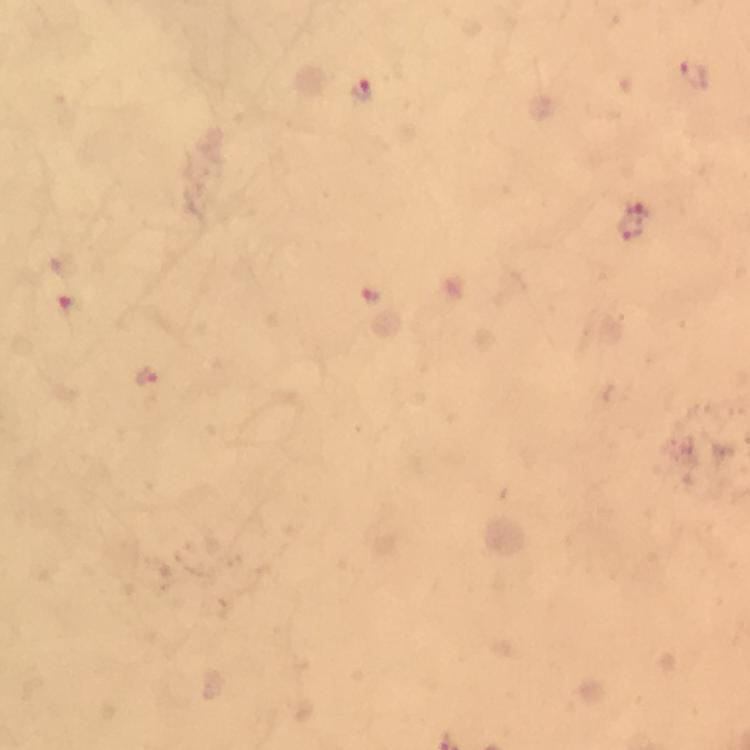
Approximate centers as (x, y) in pixels. Plasmodium parasite locations: (697, 76), (362, 90), (633, 221), (369, 296), (68, 305), (150, 379). Immersion oil applied. 100x magnification. Giemsa stain. Thick blood smear. A crop from one field of view. From a malaria diagnostic workup. Image is 750×750 pixels. Photographed with a smartphone mounted on the microscope.